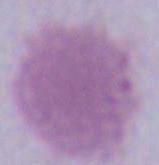

Micrograph. An erythrocyte is shown. 1000x magnification.